Point out each malaria parasite.
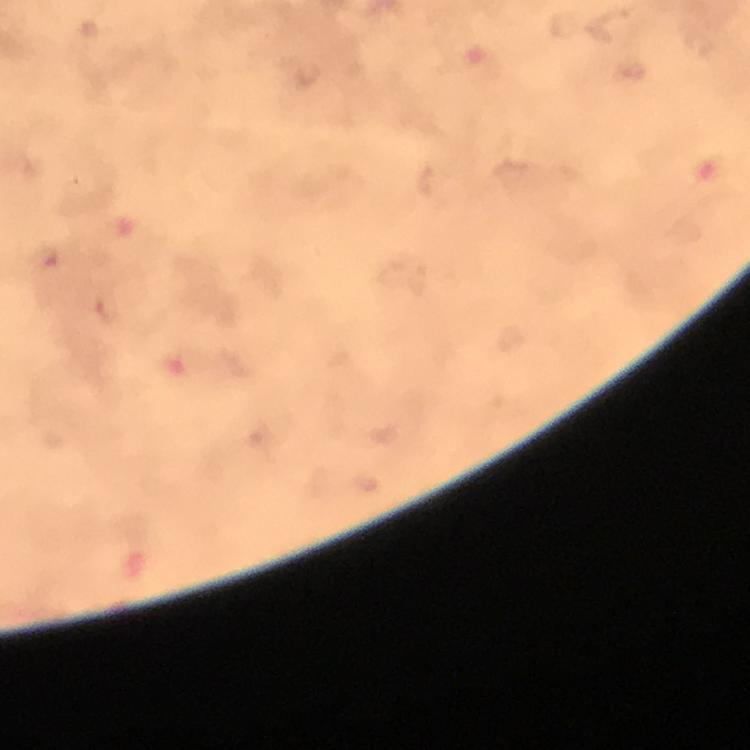

Approximate object centers, in pixels from the top-left corner.
Malaria parasites: (x=46, y=258), (x=108, y=309).

Image is 750×750 pixels. Cropped region of a single field of view. Immersion oil applied. Smartphone photograph taken through a microscope. Thick blood smear. Giemsa-stained preparation. From a diagnostic examination for malaria. At 100x magnification.